Classify this cell by malaria status.
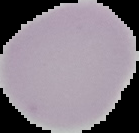
It is uninfected.

{
  "image_size": "139×133 pixels",
  "preparation": "thin blood smear",
  "image_type": "segmented cell region with the area outside set to black"
}